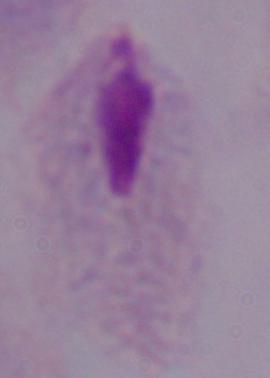
{
  "identification": "trichomonad",
  "magnification": "1000x",
  "modality": "photomicrograph"
}